State which parasite is depicted.
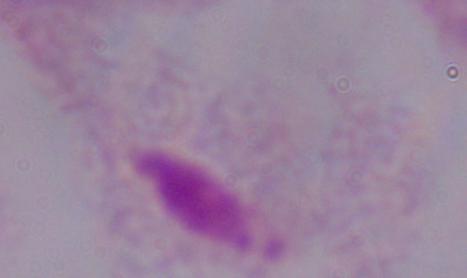

A trichomonad.

magnification = 1000x
modality = photomicrograph